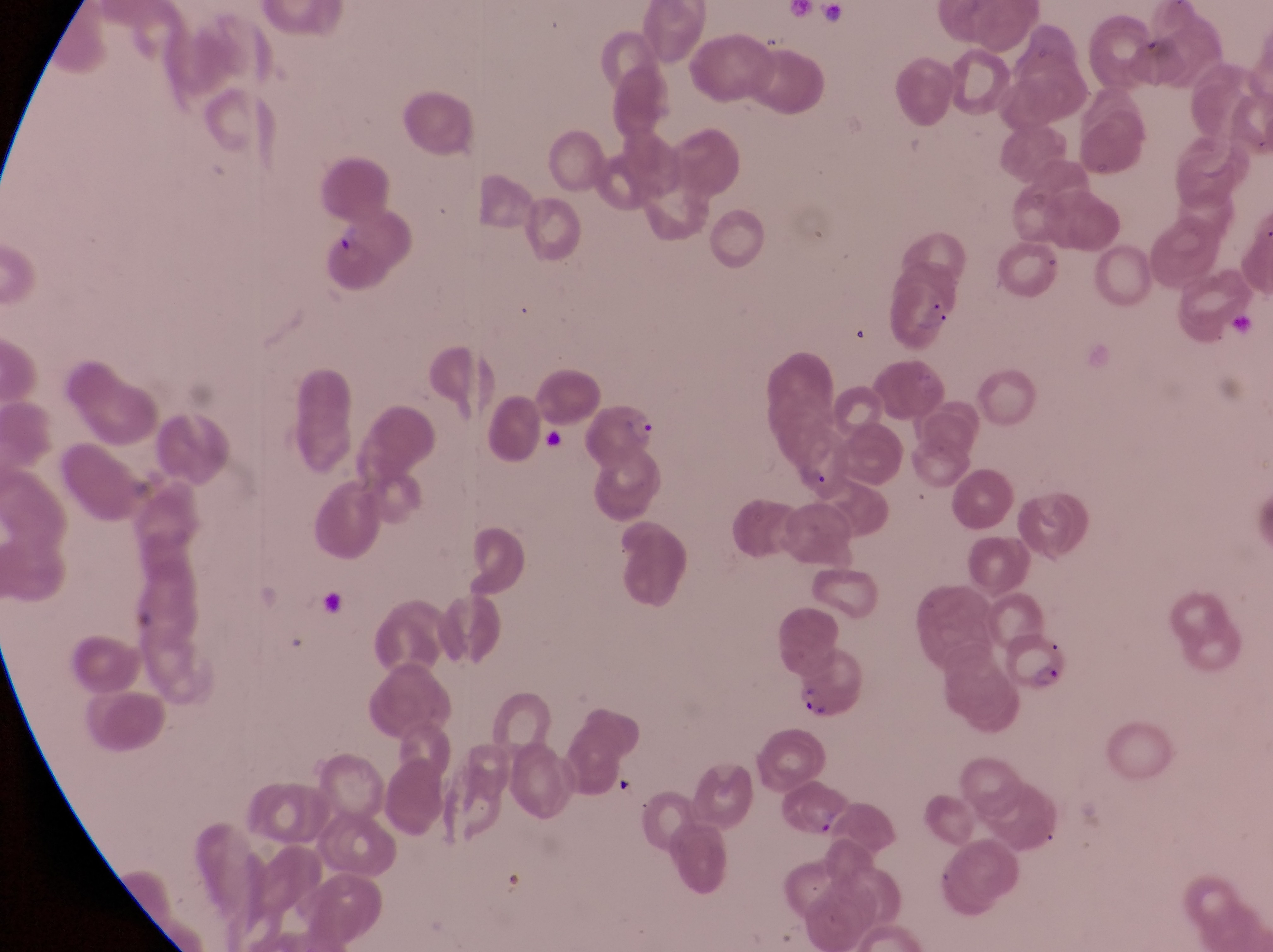

Approximate bounding boxes as left top right bottom in pixels.
Summary:
  - Trophozoite locations: 330 223 367 256
  - Parasitised red blood cell locations: 584 397 662 467; 1008 627 1071 694; 791 651 866 723
  - Image size: 1273×952 pixels
  - Country: Uganda
  - Preparation: thin blood smear
  - Magnification: 1000x
  - Capture: smartphone photograph through the eyepiece of an Olympus CX-23 microscope
  - Field of view: single